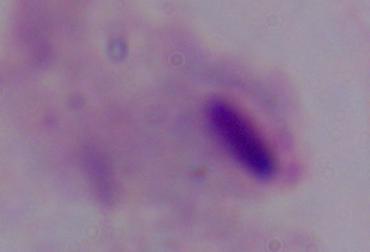

modality = micrograph
magnification = 1000x
identification = trichomonad